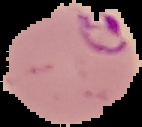

Result: malaria parasites identified. From a thin blood smear. Image is 142×127 pixels. Cell region segmented out of the field of view; the surrounding area is masked to black.